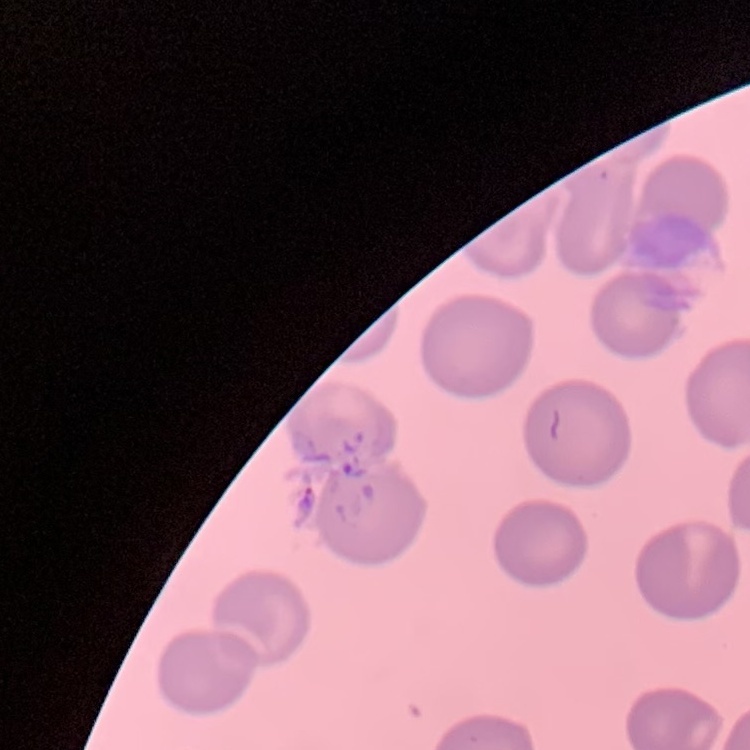
red_blood_cell_morphology: no rouleaux formation
stain: Field's or Giemsa
image_type: square crop of a larger photomicrograph
preparation: thin peripheral smear